Locate every blood parasite and identify its species.
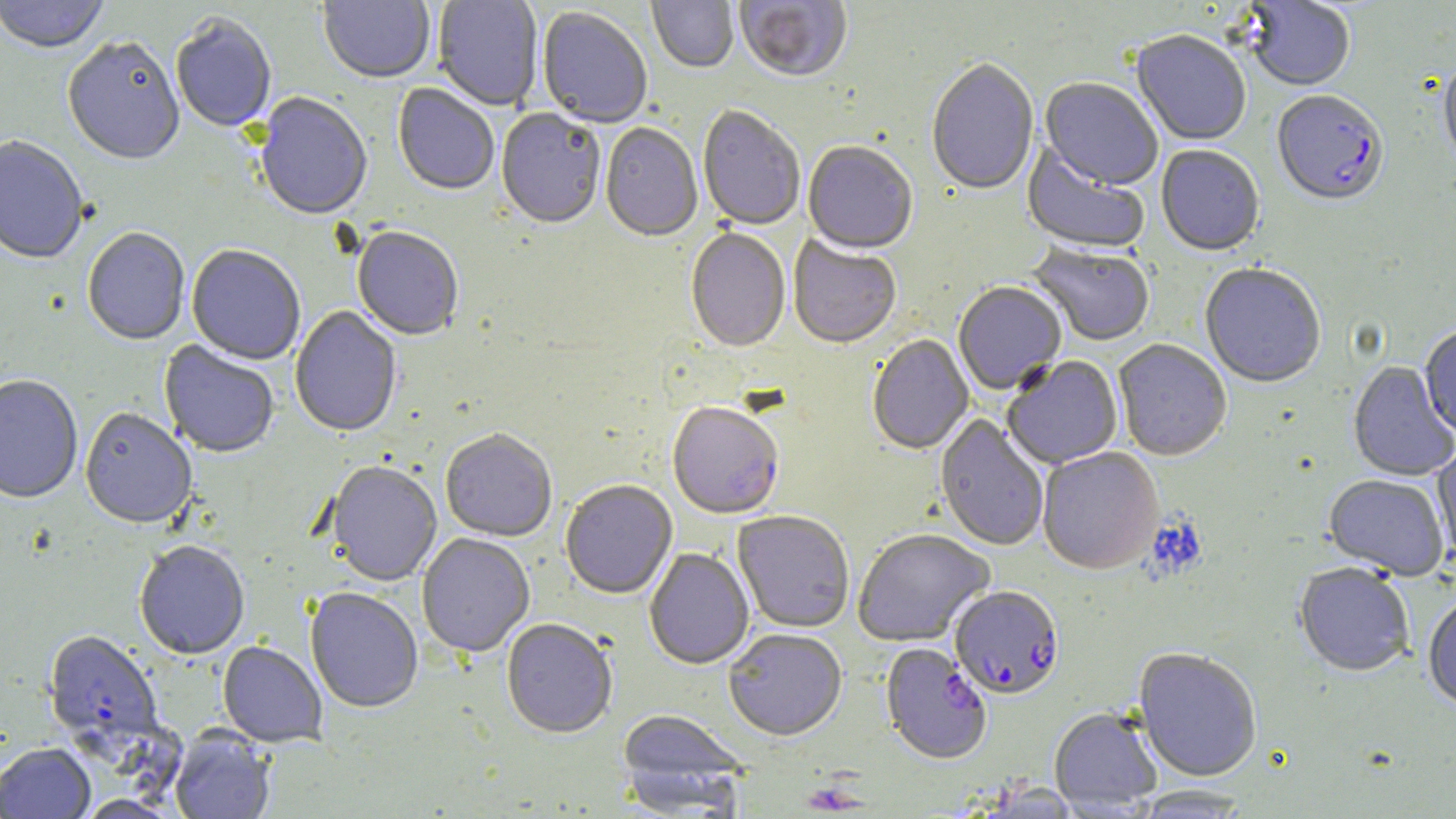
Approximate bounding boxes as named x1/y1/x2/y2 corners in pixels.
Plasmodium falciparum-infected red blood cells: (x1=1272, y1=92, x2=1389, y2=210), (x1=950, y1=588, x2=1065, y2=701), (x1=42, y1=632, x2=164, y2=751), (x1=880, y1=644, x2=993, y2=767).
No Plasmodium ovale, Plasmodium malariae, Plasmodium vivax, Babesia divergens, or Trypanosoma brucei observed.

Summary:
  - Uninfected red blood cell locations: (x1=0, y1=0, x2=108, y2=57), (x1=318, y1=0, x2=435, y2=85), (x1=433, y1=0, x2=544, y2=112), (x1=647, y1=0, x2=739, y2=74), (x1=735, y1=0, x2=853, y2=84), (x1=1243, y1=1, x2=1356, y2=93), (x1=536, y1=8, x2=652, y2=130), (x1=170, y1=16, x2=277, y2=134), (x1=1131, y1=32, x2=1251, y2=147), (x1=63, y1=39, x2=185, y2=168), (x1=926, y1=61, x2=1040, y2=198), (x1=1439, y1=62, x2=1456, y2=178), (x1=1038, y1=79, x2=1162, y2=192), (x1=392, y1=84, x2=500, y2=197), (x1=254, y1=94, x2=373, y2=223), (x1=697, y1=106, x2=805, y2=232), (x1=496, y1=108, x2=605, y2=231), (x1=600, y1=124, x2=702, y2=244), (x1=0, y1=138, x2=89, y2=267), (x1=803, y1=142, x2=918, y2=257), (x1=1021, y1=143, x2=1149, y2=256), (x1=1156, y1=146, x2=1265, y2=258), (x1=82, y1=229, x2=190, y2=347), (x1=352, y1=229, x2=464, y2=342), (x1=685, y1=231, x2=790, y2=354), (x1=788, y1=237, x2=901, y2=350), (x1=1028, y1=244, x2=1155, y2=348), (x1=187, y1=247, x2=305, y2=366), (x1=1200, y1=265, x2=1327, y2=389), (x1=953, y1=283, x2=1067, y2=396), (x1=290, y1=306, x2=402, y2=439), (x1=1419, y1=327, x2=1456, y2=439), (x1=867, y1=335, x2=975, y2=456), (x1=1113, y1=340, x2=1232, y2=462), (x1=158, y1=342, x2=279, y2=459), (x1=1002, y1=356, x2=1123, y2=470), (x1=1348, y1=362, x2=1456, y2=482), (x1=0, y1=377, x2=83, y2=506), (x1=667, y1=404, x2=784, y2=521), (x1=80, y1=410, x2=197, y2=531), (x1=934, y1=415, x2=1049, y2=552), (x1=441, y1=431, x2=557, y2=543), (x1=1431, y1=445, x2=1456, y2=561), (x1=1037, y1=449, x2=1164, y2=576), (x1=326, y1=462, x2=442, y2=588), (x1=1323, y1=475, x2=1449, y2=582), (x1=560, y1=481, x2=677, y2=600), (x1=733, y1=512, x2=854, y2=634), (x1=852, y1=531, x2=996, y2=648), (x1=417, y1=534, x2=535, y2=660), (x1=134, y1=543, x2=250, y2=661), (x1=644, y1=549, x2=755, y2=671), (x1=1294, y1=565, x2=1414, y2=680), (x1=304, y1=588, x2=423, y2=715), (x1=1423, y1=596, x2=1456, y2=713), (x1=501, y1=620, x2=617, y2=740), (x1=724, y1=631, x2=847, y2=744), (x1=217, y1=642, x2=327, y2=748), (x1=1132, y1=649, x2=1262, y2=784), (x1=1049, y1=709, x2=1162, y2=814), (x1=617, y1=710, x2=748, y2=809), (x1=169, y1=728, x2=275, y2=819), (x1=0, y1=744, x2=96, y2=818), (x1=1130, y1=786, x2=1253, y2=817)
  - Slide-level diagnosis: Plasmodium falciparum
  - Image size: 1456×819 pixels
  - Field of view: single
  - Magnification: 1000x
  - Modality: light microscopy
  - Stain: May-Grünwald-Giemsa
  - Preparation: thin blood smear